Assess this cell for malaria.
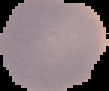

Uninfected.

Summary:
  - Image size: 109×91 pixels
  - Preparation: thin blood smear
  - Image type: cell region segmented out of the field of view; surrounding area masked to black